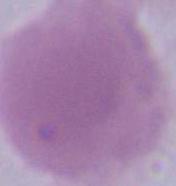 Photomicrograph. An erythrocyte is shown. Captured at 1000x magnification.